Report the malaria status of this cell.
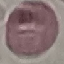
Uninfected.

Summary:
  - Capture: smartphone camera at the microscope eyepiece
  - Stain: Giemsa
  - Image type: automatically extracted cell patch, resized to 64 × 64 pixels
  - Preparation: thin smear